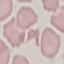
Summary:
  - Result: negative for malaria parasites
  - Stain: Giemsa
  - Image type: cell patch, automatically extracted from a larger field of view and resized to 64 × 64 pixels
  - Capture: smartphone through the microscope eyepiece
  - Preparation: thin blood smear